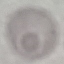

{
  "result": "no malaria parasites seen",
  "capture": "smartphone through the microscope eyepiece",
  "preparation": "thin smear",
  "stain": "Giemsa",
  "image_type": "automatically extracted cell patch, resized to 64 × 64 pixels"
}